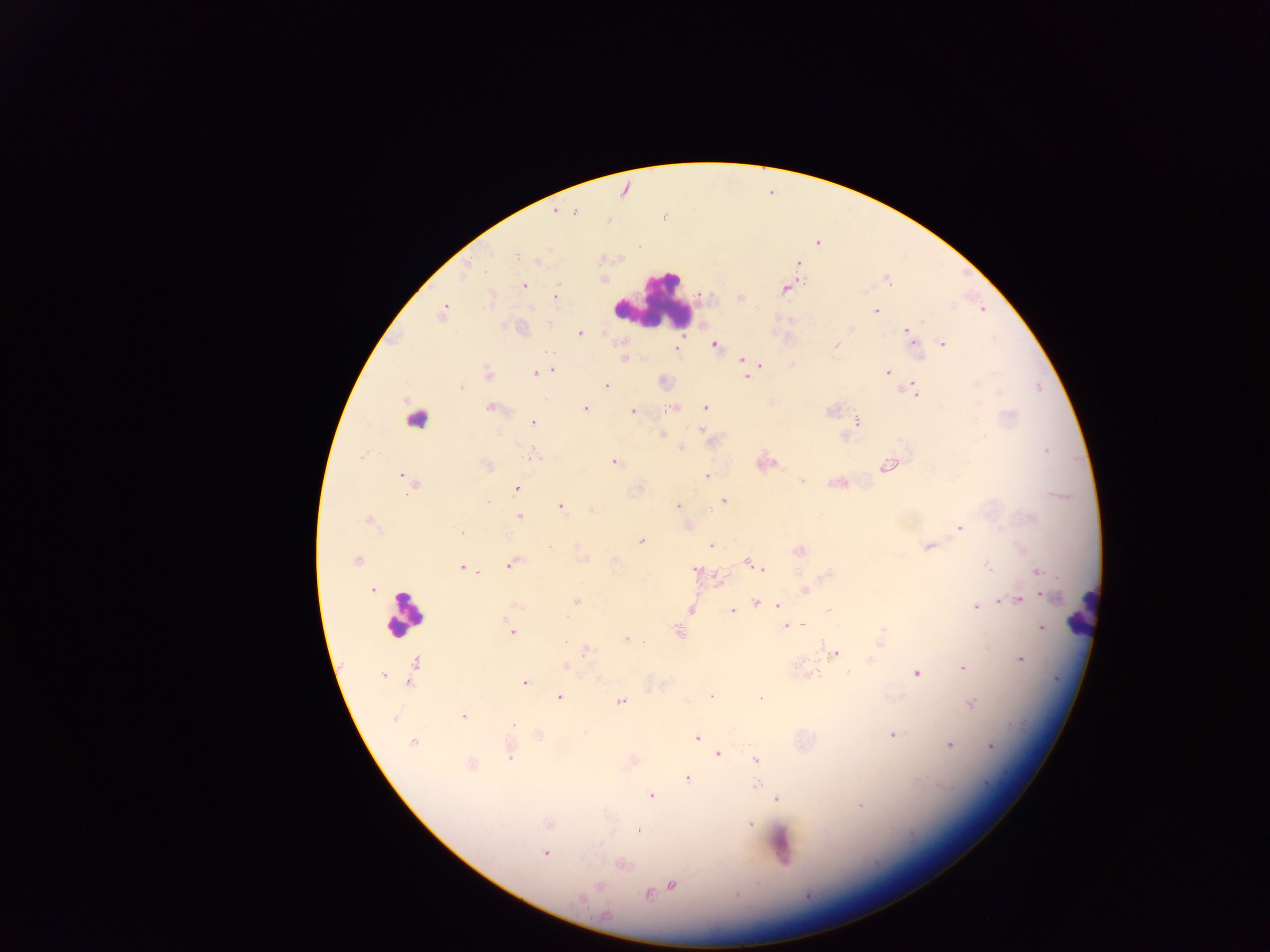

Approximate centers as x y in pixels.
Summary:
  - Plasmodium parasite locations: 574 210; 556 212; 817 243; 516 255; 538 259; 798 263; 885 277; 603 279; 524 285; 786 287; 555 297; 741 298; 875 311; 443 312; 550 321; 851 329; 909 332; 579 333; 942 344; 714 345; 835 345; 677 348; 623 359; 742 360; 758 366; 551 370; 888 372; 535 373; 487 374; 748 375; 663 381; 606 385; 460 386; 912 391; 772 402; 490 407; 584 408; 672 408; 705 408; 632 410; 857 420; 532 422; 703 430; 661 434; 680 447; 536 455; 614 462; 763 463; 888 465; 486 466; 707 476; 404 478; 801 480; 838 482; 411 483; 516 489; 722 501; 560 506; 678 506; 592 510; 518 517; 369 521; 686 526; 960 526; 462 533; 640 540; 711 545; 929 546; 799 551; 582 558; 356 560; 747 561; 512 563; 462 567; 987 567; 764 569; 695 570; 1037 572; 827 574; 717 581; 373 590; 804 591; 1012 599; 1017 599; 1000 600; 576 601; 756 602; 775 604; 514 605; 976 607; 690 608; 830 609; 731 611; 785 626; 1042 629; 677 630; 511 631; 881 636; 627 639; 586 649; 835 652; 870 660; 1020 660; 415 664; 565 665; 964 667; 916 672; 383 675; 807 676; 598 677; 411 681; 525 682; 711 696; 559 697; 620 701; 971 704; 463 716; 392 718; 513 725; 539 734; 893 734; 697 739; 413 742; 949 745; 991 747; 510 751; 718 753; 757 759; 471 764; 686 777; 756 783; 651 795; 776 798; 861 805; 549 823; 749 824; 638 831; 544 853; 620 864; 671 885; 647 893
  - Leukocyte locations: 655 301; 415 423; 1082 613; 405 614; 780 844
  - Field of view: single
  - Preparation: thick blood smear
  - Image size: 1270×952 pixels
  - Country: Ghana
  - Capture: mobile-phone photograph through a microscope